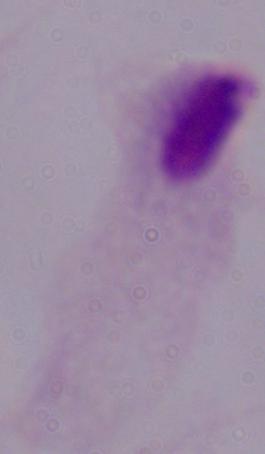

identification = trichomonad
modality = micrograph
magnification = 1000x